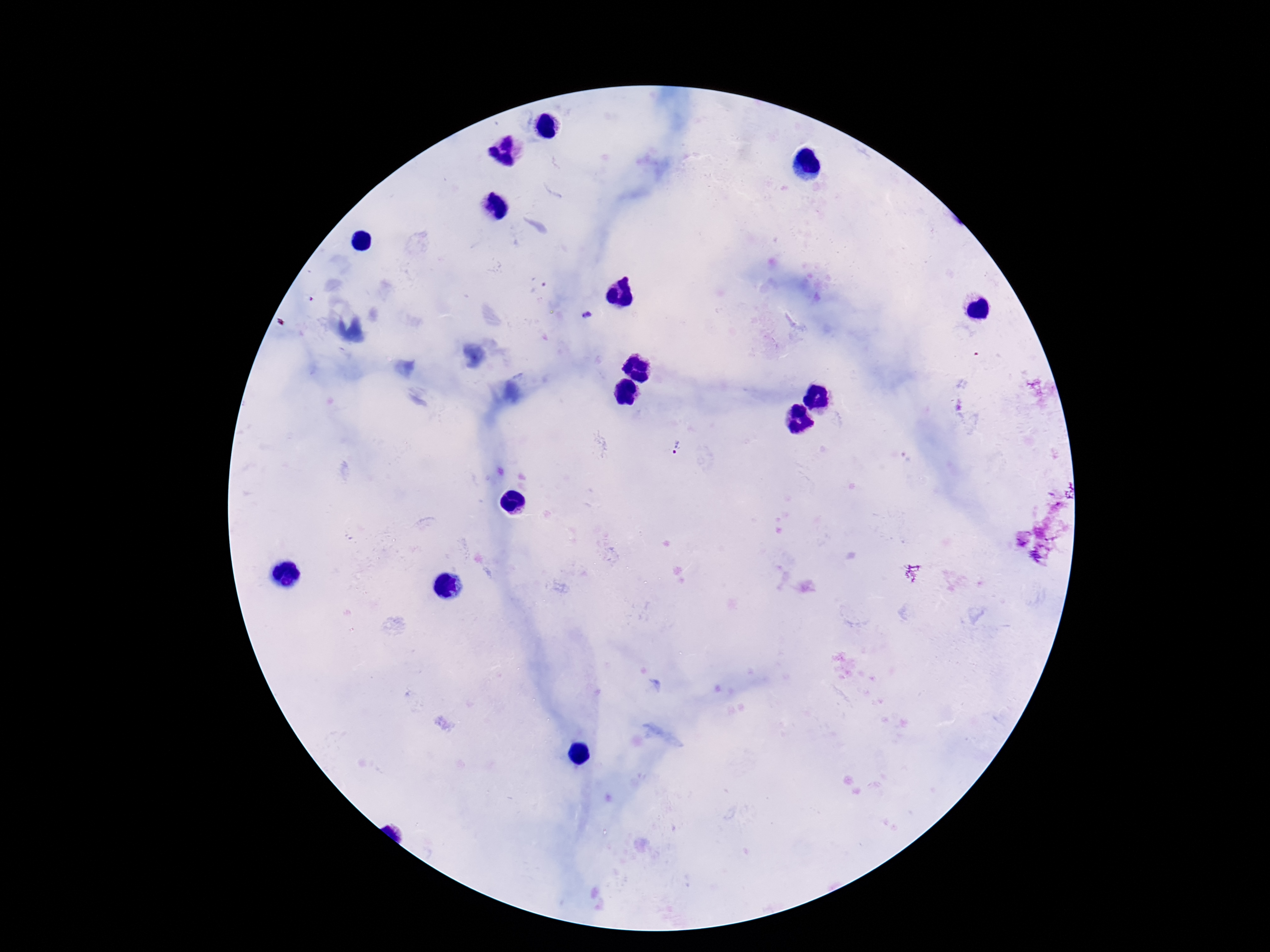
Approximate centers as {x, y} in pixels. Plasmodium parasite locations: {587, 316}, {678, 449}. Giemsa stain. Single field of view. Image is 1270×952 pixels. 100x magnification. Photographed through the microscope eyepiece with a smartphone camera. Thick peripheral-blood smear. Patient malaria status: infected.